Report the malaria status of this cell.
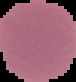

It is uninfected.

Summary:
  - Preparation: thin blood film
  - Image type: cell region segmented out of the field of view; surrounding area masked to black
  - Image size: 76×82 pixels